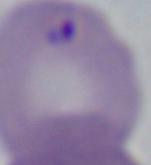

Photomicrograph. Captured at 1000x magnification. A Babesia parasite is seen.